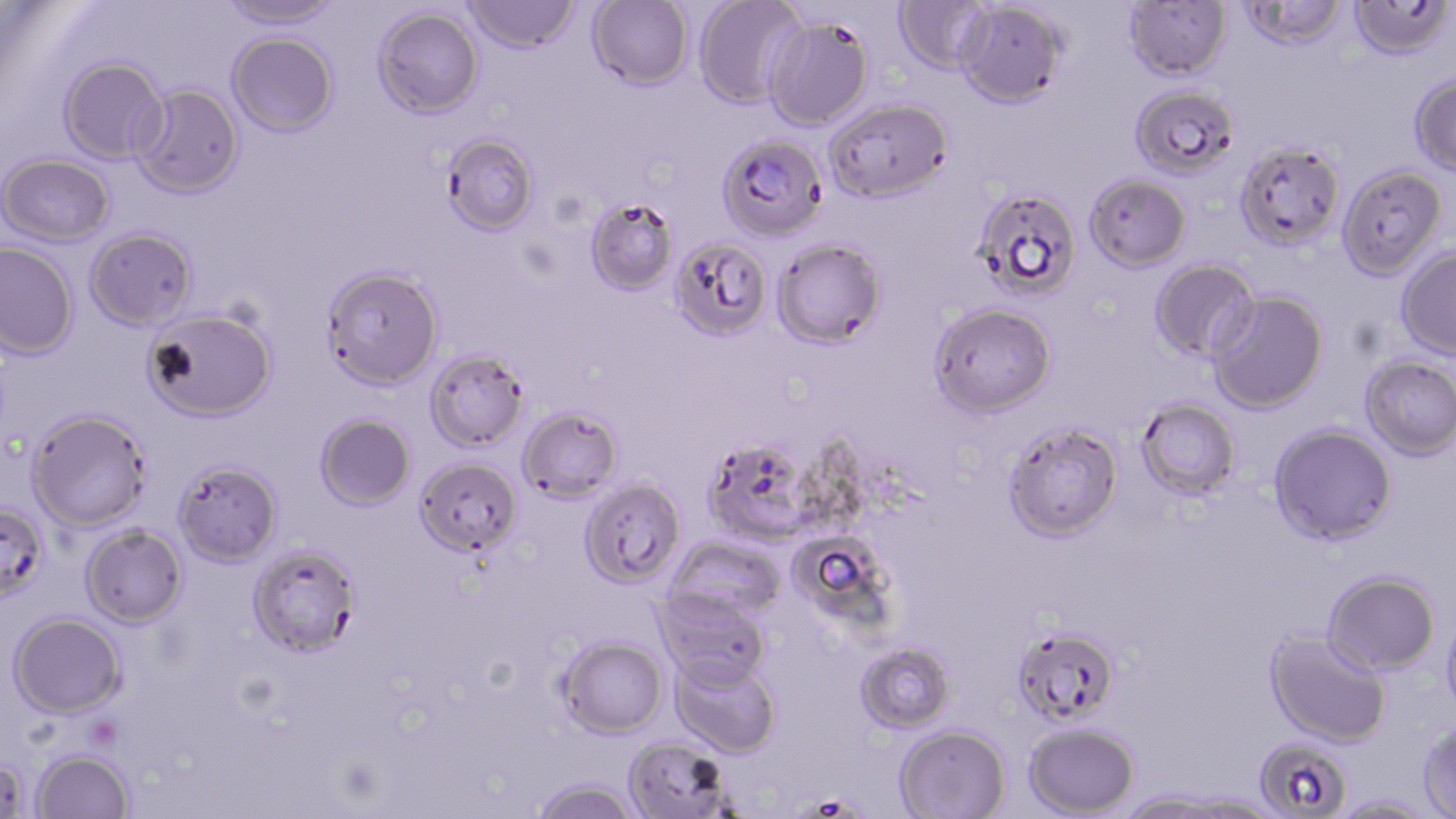

Approximate bounding boxes as (x1, y1, x2, y2) in pixels. Platelet locations: (86, 715, 122, 749), (806, 796, 861, 819). Uninfected red blood cell locations: (220, 0, 344, 29), (462, 0, 580, 54), (694, 0, 807, 109), (894, 0, 994, 75), (1124, 0, 1231, 80), (1238, 0, 1349, 51), (1349, 0, 1454, 59), (587, 1, 693, 90), (955, 1, 1066, 109), (373, 7, 484, 118), (763, 17, 874, 131), (227, 32, 338, 137), (58, 57, 169, 164), (1409, 73, 1456, 175), (130, 84, 243, 197), (1130, 85, 1240, 180), (824, 99, 952, 204), (440, 132, 539, 236), (717, 133, 828, 242), (1234, 140, 1345, 250), (0, 154, 115, 246), (1337, 164, 1447, 279), (1084, 173, 1192, 272), (972, 187, 1082, 301), (585, 199, 679, 296), (85, 227, 197, 330), (670, 237, 773, 341), (772, 239, 887, 350), (0, 242, 79, 360), (1395, 246, 1456, 361), (1149, 259, 1260, 363), (321, 267, 444, 391), (1207, 291, 1329, 414), (929, 303, 1057, 418), (141, 308, 278, 422), (425, 349, 530, 452), (1360, 355, 1456, 460), (1135, 398, 1242, 502), (517, 407, 623, 503), (27, 410, 152, 532), (315, 413, 415, 511), (1002, 421, 1124, 542), (1269, 423, 1398, 545), (704, 438, 817, 546), (414, 456, 523, 557), (173, 460, 283, 566), (580, 478, 687, 588), (0, 500, 48, 604), (80, 524, 188, 628), (665, 535, 786, 623), (791, 541, 904, 628), (247, 544, 363, 658), (1323, 570, 1441, 675), (654, 589, 772, 691), (1441, 608, 1456, 724), (9, 611, 127, 719), (1012, 626, 1120, 726), (1265, 630, 1392, 747), (557, 636, 669, 738), (855, 643, 955, 734), (670, 653, 781, 758), (1418, 719, 1456, 819), (1024, 723, 1139, 818), (894, 725, 1010, 819), (1253, 737, 1353, 818), (623, 738, 733, 819), (30, 748, 135, 818), (0, 755, 32, 817), (531, 778, 643, 819), (1114, 790, 1258, 819), (1328, 794, 1441, 818). Slide-level diagnosis: Plasmodium falciparum. 1000x magnification. Thin blood film. Image is 1456×819 pixels. May-Grünwald-Giemsa stain. Optical microscopy. One field of a larger specimen.